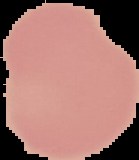 The area outside the segmented cell region is set to black. Result: negative for malaria parasites. From a thin blood film. Image is 139×160 pixels.